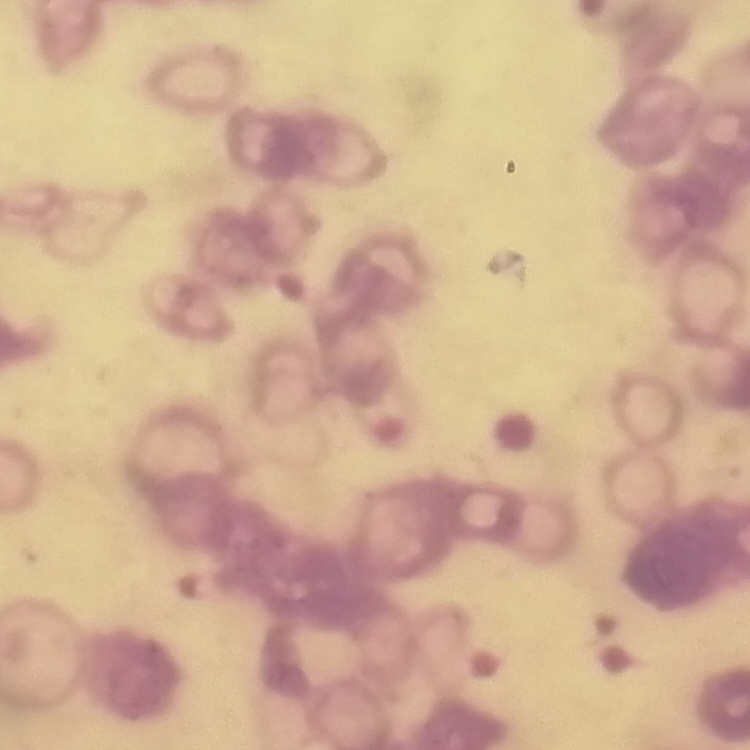
red blood cell morphology = rouleaux formation
image type = square crop of a larger photomicrograph
preparation = thin blood smear
stain = Field's or Giemsa